Locate every blood parasite and identify its species.
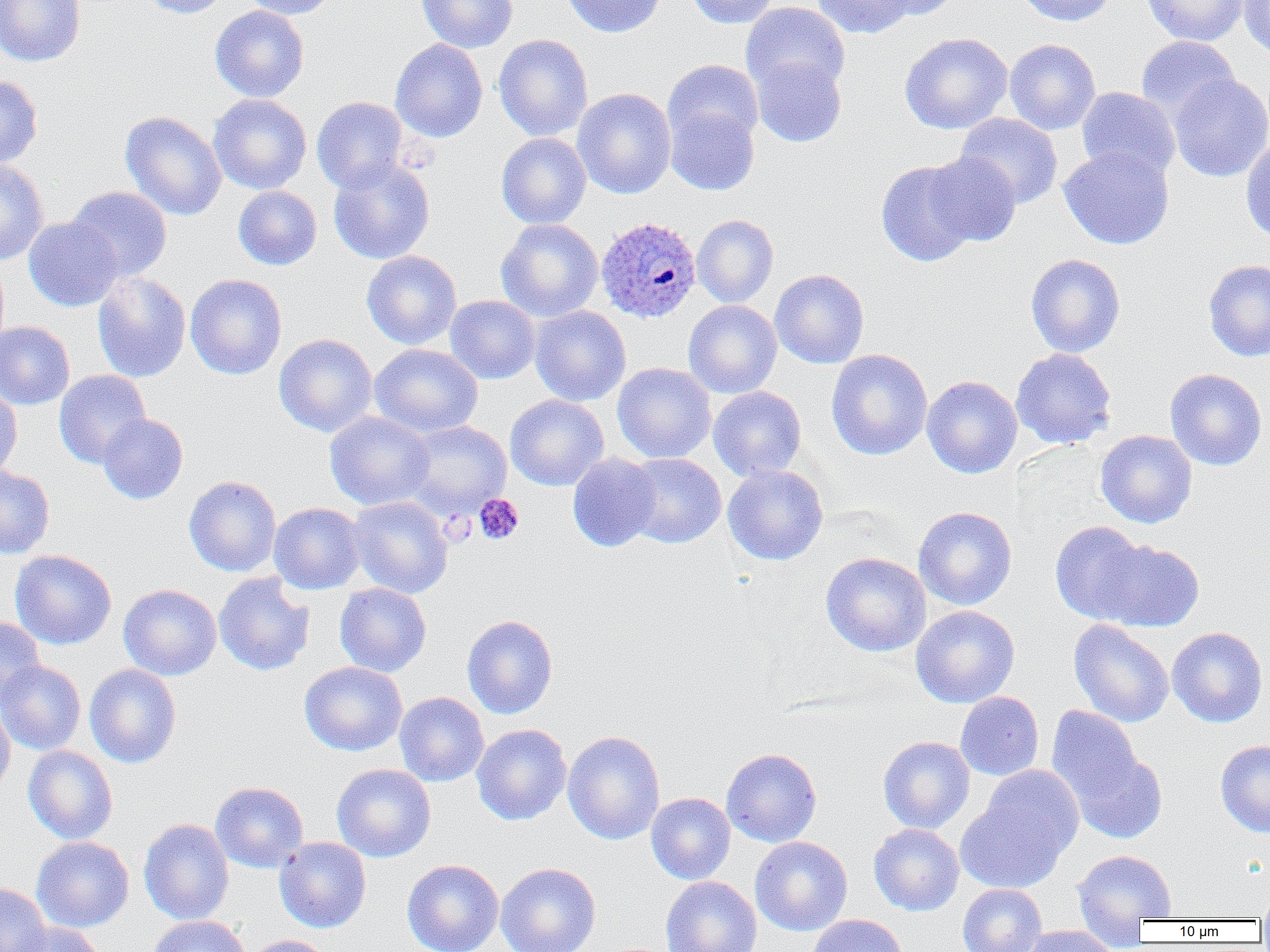
Approximate bounding boxes as named x1/y1/x2/y2 corners in pixels.
Plasmodium ovale-infected red blood cells: (x1=596, y1=217, x2=702, y2=323).
No Plasmodium falciparum, Plasmodium malariae, Plasmodium vivax, Babesia divergens, or Trypanosoma brucei observed.

Platelet locations: (x1=473, y1=493, x2=524, y2=545). Uninfected red blood cell locations: (x1=1, y1=0, x2=85, y2=67), (x1=139, y1=0, x2=232, y2=18), (x1=239, y1=0, x2=337, y2=19), (x1=416, y1=0, x2=517, y2=53), (x1=562, y1=0, x2=666, y2=38), (x1=685, y1=0, x2=781, y2=28), (x1=812, y1=0, x2=915, y2=38), (x1=873, y1=0, x2=962, y2=21), (x1=1014, y1=0, x2=1117, y2=27), (x1=1141, y1=0, x2=1249, y2=47), (x1=1238, y1=1, x2=1270, y2=60), (x1=741, y1=2, x2=850, y2=97), (x1=210, y1=5, x2=310, y2=102), (x1=899, y1=32, x2=1012, y2=134), (x1=494, y1=34, x2=593, y2=141), (x1=1137, y1=36, x2=1240, y2=125), (x1=390, y1=39, x2=488, y2=142), (x1=1004, y1=39, x2=1101, y2=134), (x1=750, y1=55, x2=846, y2=147), (x1=662, y1=59, x2=763, y2=150), (x1=1168, y1=73, x2=1270, y2=182), (x1=0, y1=74, x2=43, y2=169), (x1=1077, y1=87, x2=1180, y2=182), (x1=572, y1=88, x2=676, y2=199), (x1=208, y1=94, x2=312, y2=195), (x1=312, y1=96, x2=408, y2=194), (x1=665, y1=105, x2=759, y2=196), (x1=120, y1=111, x2=226, y2=221), (x1=955, y1=113, x2=1063, y2=209), (x1=496, y1=132, x2=591, y2=229), (x1=1240, y1=136, x2=1270, y2=244), (x1=1058, y1=147, x2=1174, y2=250), (x1=924, y1=153, x2=1021, y2=246), (x1=328, y1=159, x2=435, y2=264), (x1=876, y1=159, x2=978, y2=267), (x1=0, y1=160, x2=49, y2=266), (x1=67, y1=186, x2=172, y2=281), (x1=233, y1=186, x2=322, y2=270), (x1=692, y1=214, x2=779, y2=308), (x1=23, y1=216, x2=123, y2=311), (x1=496, y1=218, x2=603, y2=322), (x1=361, y1=250, x2=461, y2=349), (x1=1025, y1=253, x2=1126, y2=357), (x1=1203, y1=259, x2=1270, y2=362), (x1=770, y1=269, x2=869, y2=368), (x1=92, y1=271, x2=191, y2=382), (x1=185, y1=274, x2=287, y2=379), (x1=445, y1=295, x2=540, y2=384), (x1=683, y1=300, x2=782, y2=398), (x1=529, y1=305, x2=631, y2=406), (x1=0, y1=321, x2=75, y2=410), (x1=274, y1=333, x2=378, y2=437), (x1=370, y1=343, x2=483, y2=438), (x1=1011, y1=348, x2=1117, y2=449), (x1=826, y1=349, x2=933, y2=460), (x1=613, y1=362, x2=716, y2=463), (x1=1164, y1=368, x2=1267, y2=471), (x1=53, y1=370, x2=151, y2=469), (x1=921, y1=376, x2=1022, y2=479), (x1=0, y1=384, x2=22, y2=482), (x1=708, y1=386, x2=807, y2=481), (x1=505, y1=394, x2=609, y2=491), (x1=325, y1=412, x2=435, y2=510), (x1=97, y1=413, x2=188, y2=504), (x1=402, y1=420, x2=511, y2=517), (x1=1095, y1=430, x2=1197, y2=528), (x1=567, y1=452, x2=662, y2=552), (x1=621, y1=453, x2=726, y2=548), (x1=722, y1=464, x2=828, y2=566), (x1=0, y1=466, x2=55, y2=558), (x1=184, y1=476, x2=281, y2=577), (x1=347, y1=496, x2=453, y2=599), (x1=268, y1=502, x2=366, y2=595), (x1=913, y1=506, x2=1017, y2=610), (x1=1049, y1=521, x2=1151, y2=624), (x1=1097, y1=539, x2=1204, y2=632), (x1=10, y1=549, x2=117, y2=650), (x1=820, y1=552, x2=932, y2=656), (x1=214, y1=573, x2=314, y2=676), (x1=118, y1=583, x2=222, y2=680), (x1=335, y1=583, x2=431, y2=677), (x1=910, y1=605, x2=1020, y2=708), (x1=462, y1=614, x2=558, y2=719), (x1=1, y1=617, x2=45, y2=706), (x1=1068, y1=619, x2=1174, y2=727), (x1=1167, y1=627, x2=1268, y2=727), (x1=0, y1=660, x2=86, y2=755), (x1=299, y1=661, x2=408, y2=756), (x1=84, y1=664, x2=181, y2=768), (x1=955, y1=691, x2=1044, y2=780), (x1=394, y1=692, x2=489, y2=786), (x1=954, y1=697, x2=1142, y2=783), (x1=0, y1=698, x2=15, y2=797), (x1=1046, y1=706, x2=1143, y2=806), (x1=472, y1=723, x2=571, y2=825), (x1=562, y1=730, x2=665, y2=845), (x1=878, y1=736, x2=975, y2=833), (x1=1215, y1=739, x2=1270, y2=838), (x1=23, y1=745, x2=118, y2=844), (x1=721, y1=748, x2=822, y2=847), (x1=1068, y1=749, x2=1167, y2=844), (x1=331, y1=763, x2=436, y2=862), (x1=955, y1=781, x2=1075, y2=893), (x1=210, y1=782, x2=308, y2=873), (x1=646, y1=792, x2=735, y2=884), (x1=138, y1=818, x2=234, y2=925), (x1=869, y1=823, x2=964, y2=915), (x1=31, y1=836, x2=134, y2=932), (x1=750, y1=836, x2=853, y2=936), (x1=274, y1=837, x2=372, y2=933), (x1=1072, y1=849, x2=1177, y2=933), (x1=402, y1=859, x2=503, y2=952), (x1=495, y1=862, x2=601, y2=952), (x1=661, y1=876, x2=761, y2=952), (x1=0, y1=882, x2=52, y2=952), (x1=957, y1=884, x2=1046, y2=952), (x1=1256, y1=887, x2=1270, y2=923), (x1=806, y1=914, x2=909, y2=952), (x1=146, y1=915, x2=251, y2=952), (x1=12, y1=923, x2=105, y2=952), (x1=1020, y1=925, x2=1119, y2=952), (x1=244, y1=935, x2=334, y2=952). Slide-level diagnosis: Plasmodium ovale. Image is 1270×952 pixels. Single field of view. Thin blood smear. Optical microscopy. Captured at 1000x magnification.